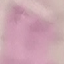
malaria status = uninfected
stain = Giemsa
capture = smartphone through the microscope eyepiece
image type = automatically extracted cell patch, resized to 64 × 64 pixels
preparation = thin smear